Evaluate for malaria.
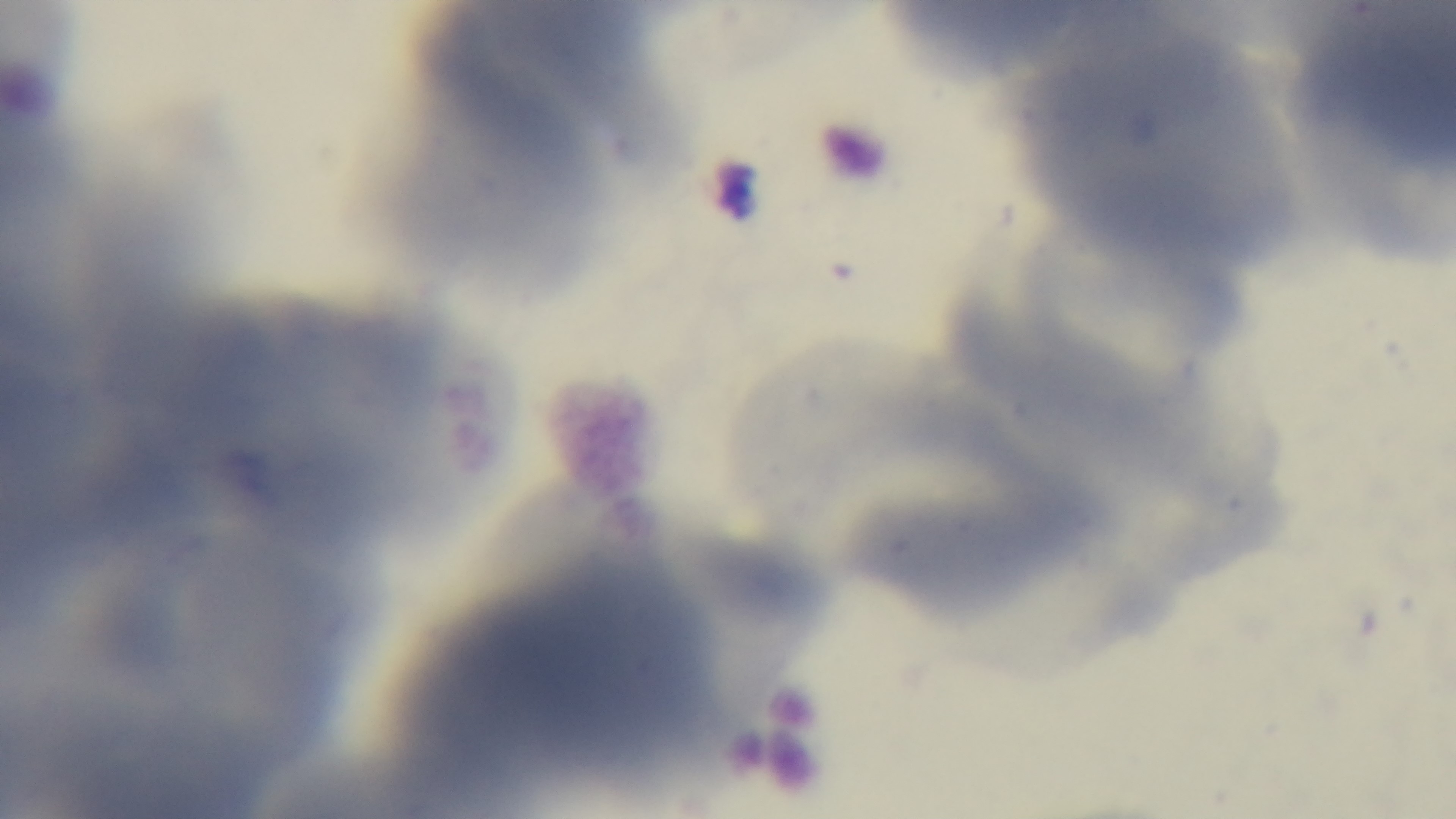

It is uninfected.

field of view = single
capture = mounted 4K digital camera
stain = Giemsa
modality = light microscopy
preparation = thin smear
objective = 100x oil immersion